Assess this cell for malaria.
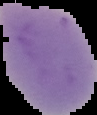

It is uninfected.

{
  "image_type": "segmented cell region with the area outside set to black",
  "image_size": "97×115 pixels",
  "preparation": "thin blood film"
}